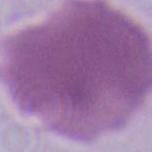

magnification: 1000x
identification: erythrocyte
modality: micrograph